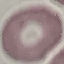 Result: negative for malaria parasites. Thin blood smear. Giemsa stain. Cell patch, automatically extracted from a larger field of view and resized to 64 × 64 pixels. Acquired by smartphone through the microscope eyepiece.